Name the blood parasite species.
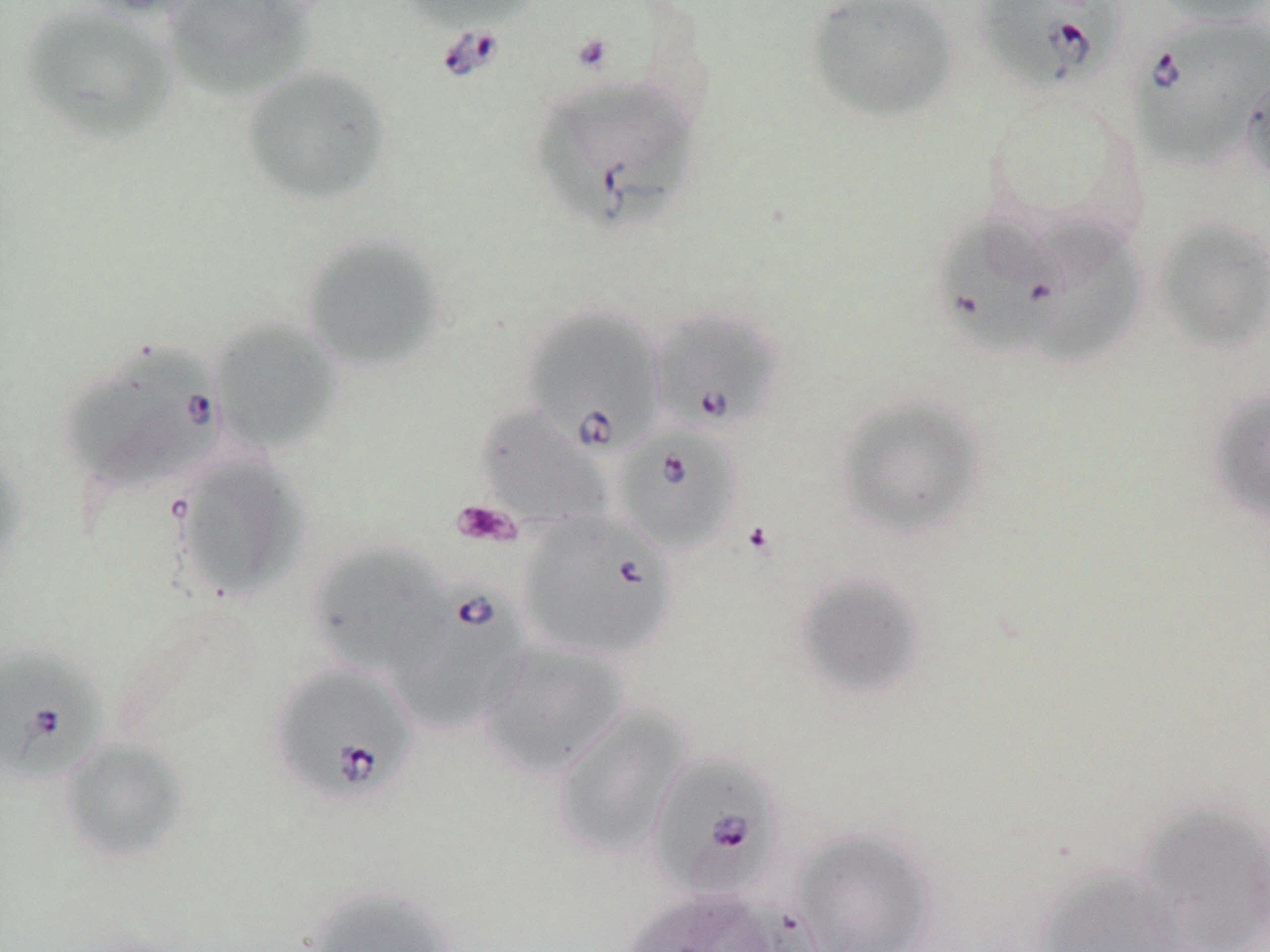

Babesia divergens.

image size = 1270×952 pixels
magnification = 1000x
field of view = one of a larger specimen
modality = light microscopy
platelet locations = approximate bounding boxes as (x1,y1)-(x2,y2) corner pairs in pixels: (570,32)-(615,74), (450,499)-(521,548)
preparation = thin blood film
Babesia divergens-infected red blood cell locations = approximate bounding boxes as (x1,y1)-(x2,y2) corner pairs in pixels: (976,0)-(1125,92), (1128,15)-(1269,171), (532,74)-(700,235), (933,212)-(1067,358), (649,306)-(783,435), (524,307)-(665,453), (63,340)-(228,497), (614,425)-(744,556), (518,511)-(678,662), (386,582)-(531,734), (0,645)-(107,786), (270,662)-(419,807), (648,751)-(785,903)
uninfected red blood cell locations = approximate bounding boxes as (x1,y1)-(x2,y2) corner pairs in pixels: (72,0)-(208,21), (161,0)-(321,102), (398,0)-(541,33), (802,0)-(959,123), (1148,0)-(1269,28), (17,3)-(182,146), (239,63)-(395,208), (1240,66)-(1270,187), (1154,217)-(1270,352), (1032,225)-(1145,367), (298,233)-(449,373), (209,317)-(344,455), (1207,388)-(1270,524), (832,392)-(989,540), (475,406)-(611,532), (0,448)-(30,583), (175,454)-(307,601), (309,543)-(446,676), (791,571)-(929,700), (478,640)-(631,779), (550,704)-(690,862), (59,738)-(189,864), (1133,799)-(1270,951), (789,828)-(940,952), (1033,868)-(1195,952), (301,885)-(458,952), (623,888)-(778,952)
stain = May-Grünwald-Giemsa